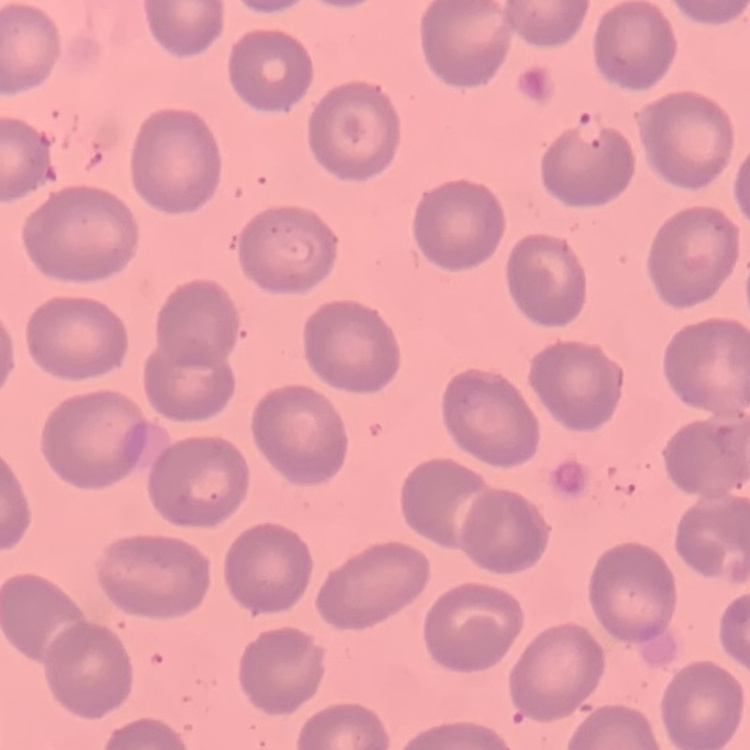 The red blood cells show no rouleaux formation. Thin peripheral smear. One tile cut from a larger photomicrograph. Stained with either Field's or Giemsa.